Report the malaria status of this cell.
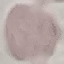

It is uninfected.

Thin blood film. Photographed with a smartphone camera at the microscope eyepiece. Giemsa-stained preparation. Automatically extracted cell patch, resized to 64 × 64 pixels.